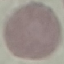

result = negative for malaria parasites
image type = cell patch, automatically extracted from a larger field of view and resized to 64 × 64 pixels
preparation = thin blood smear
capture = smartphone camera at the microscope eyepiece
stain = Giemsa